Assess this cell for malaria.
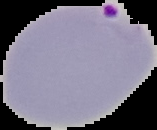

It is parasitized.

image_type: cell region segmented out of the field of view; surrounding area masked to black
image_size: 157×130 pixels
preparation: thin blood film